State which parasite is depicted.
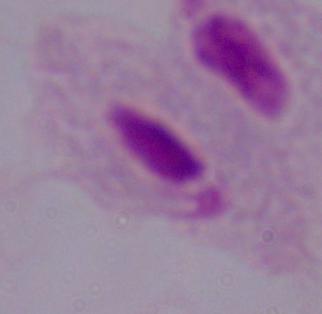

This is a trichomonad.

Summary:
  - Magnification: 1000x
  - Modality: micrograph